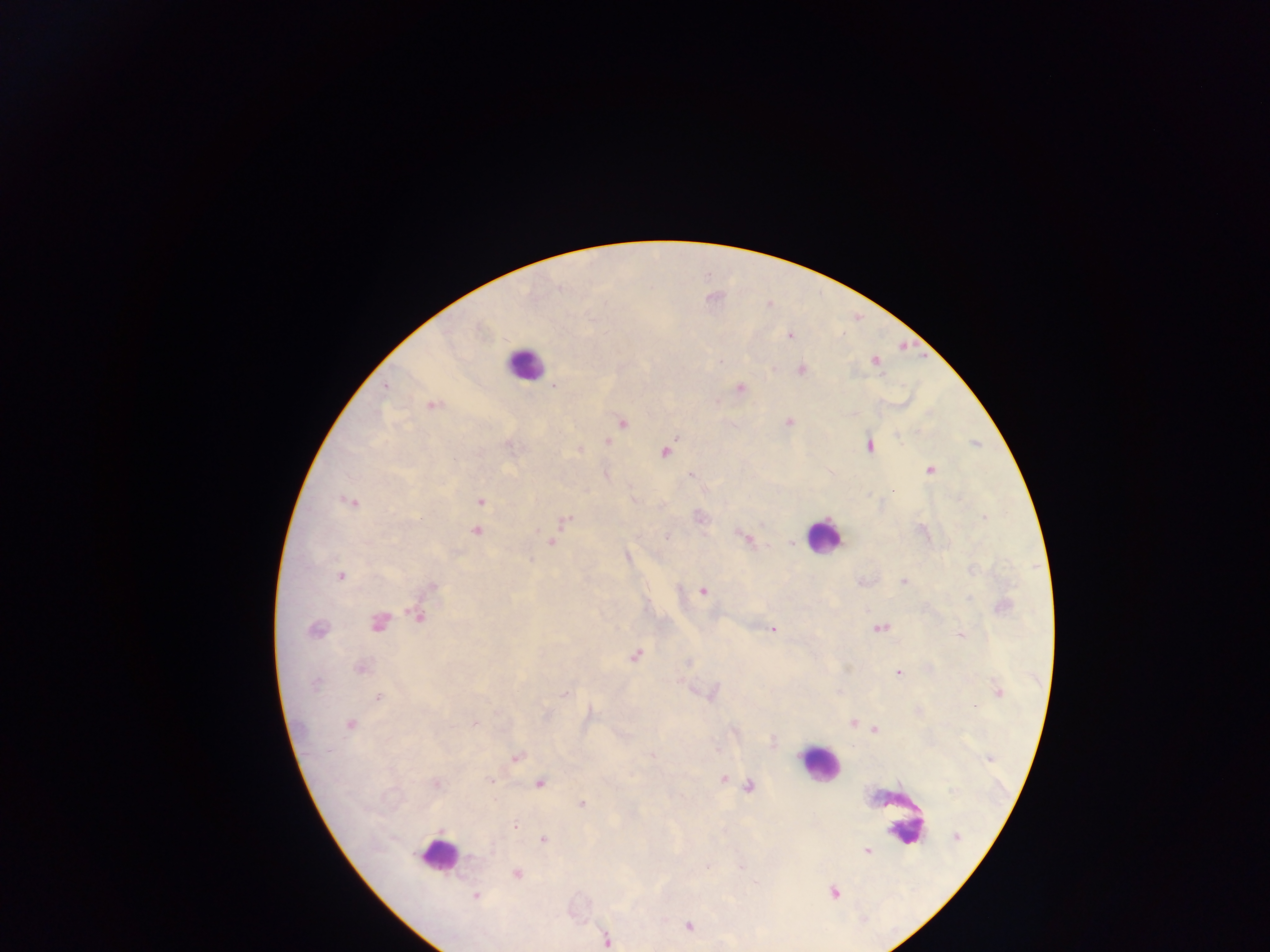
Approximate centers as (x, y) in pixels. Malaria parasite locations: (769, 305), (789, 336), (720, 362), (876, 362), (800, 370), (386, 386), (554, 386), (740, 388), (431, 405), (789, 422), (623, 423), (607, 442), (869, 446), (665, 452), (930, 470), (691, 476), (893, 490), (348, 501), (480, 501), (984, 516), (567, 519), (476, 531), (538, 531), (666, 536), (745, 539), (551, 542), (340, 576), (903, 581), (433, 586), (702, 591), (418, 617), (378, 622), (881, 628), (316, 629), (773, 629), (960, 635), (635, 656), (361, 668), (899, 673), (315, 684), (998, 691), (564, 694), (378, 698), (474, 723), (852, 723), (350, 724), (875, 730), (652, 754), (517, 758), (724, 779), (490, 780), (540, 783), (436, 784), (749, 785), (583, 804), (514, 826), (956, 836), (543, 840), (867, 851), (516, 874), (834, 893), (475, 896), (688, 926), (607, 940). Leukocyte locations: (524, 363), (822, 537), (819, 764), (895, 813), (438, 855). Thick blood film. Single field of view. Image is 1270×952 pixels. Mobile-phone photograph taken through the microscope. Collected in Ghana.